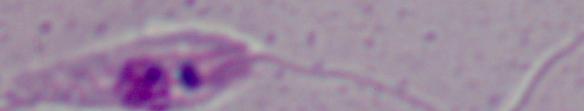
Summary:
  - Magnification: 1000x
  - Modality: photomicrograph
  - Identification: Leishmania